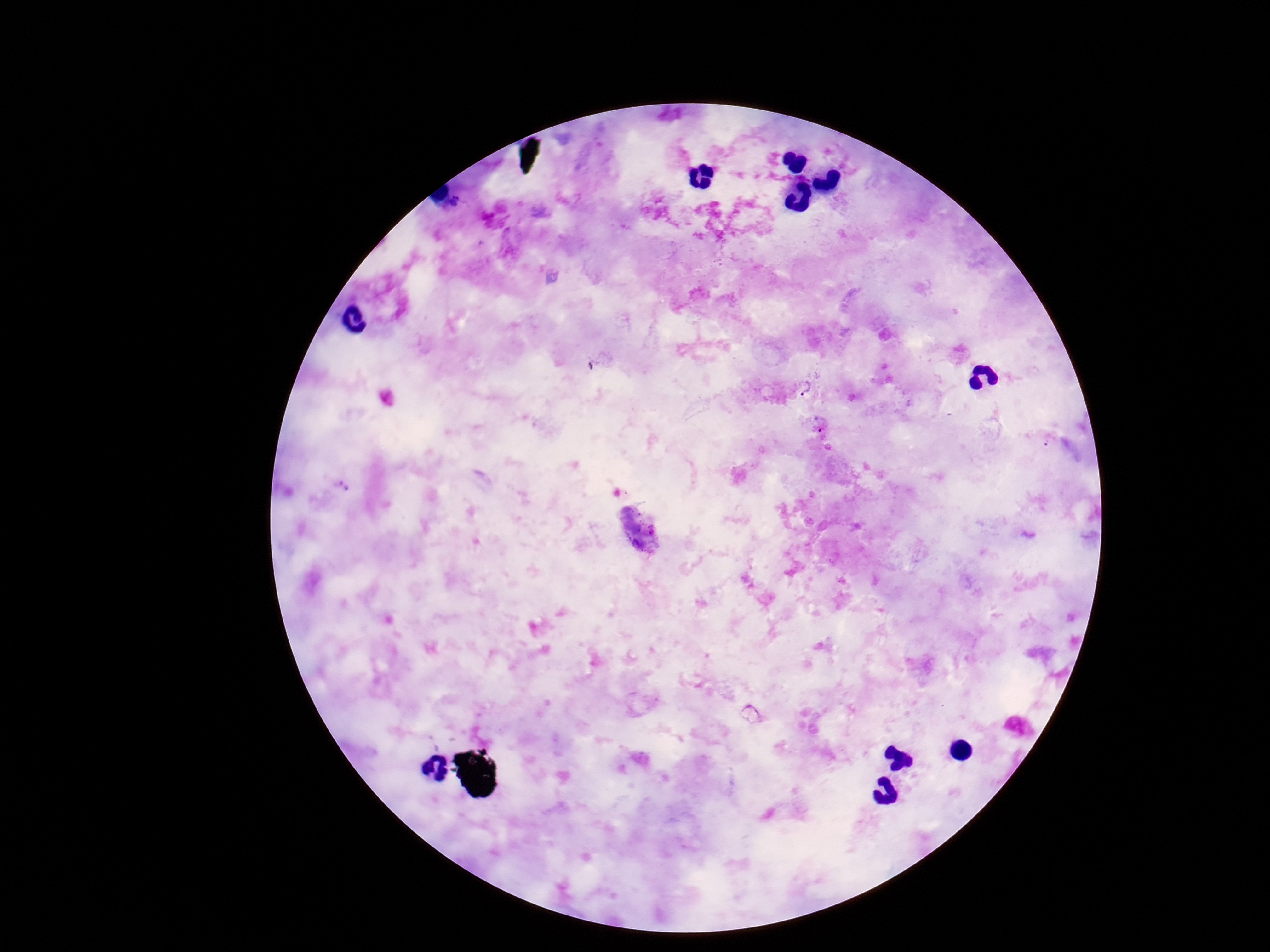

Approximate centers as (x, y) in pixels. Plasmodium parasite locations: (804, 389), (820, 422), (1050, 440), (340, 483). Image is 1270×952 pixels. Patient malaria status: positive. 100x magnification. Giemsa stain. Smartphone photograph taken through the microscope eyepiece. Thick blood film. One field from this slide.